Assess the morphology of the red blood cells.
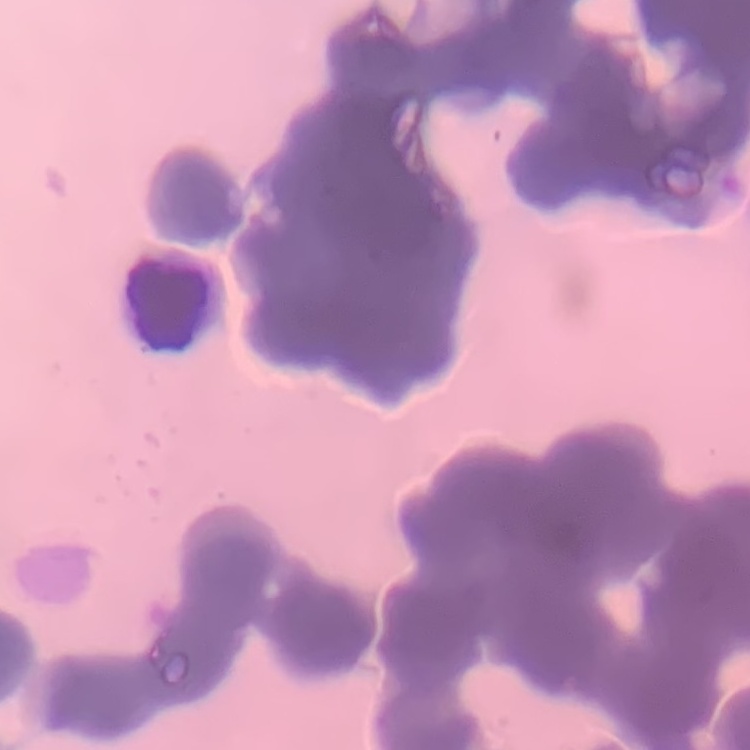
They show rouleaux formation.

Thin blood smear. Stained with either Field's or Giemsa. One tile cut from a larger photomicrograph.